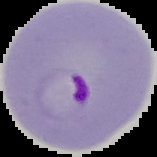

{
  "preparation": "thin blood smear",
  "result": "Plasmodium parasites identified",
  "image_size": "157×157 pixels",
  "image_type": "cell region segmented out of the field of view; surrounding area masked to black"
}